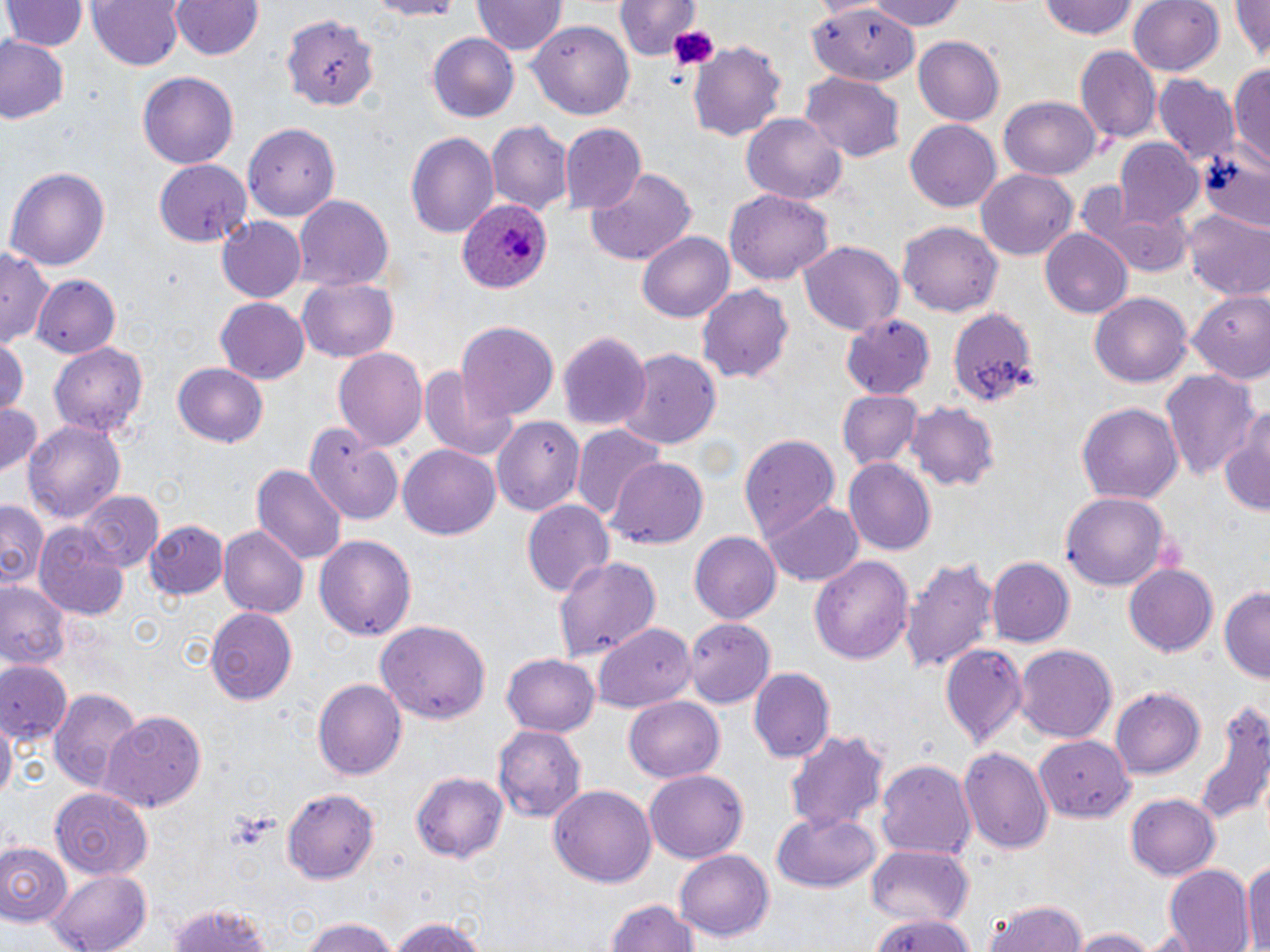

Approximate bounding boxes as named x1/y1/x2/y2 corners in pixels. Platelet locations: (x1=665, y1=22, x2=722, y2=73). Uninfected red blood cell locations: (x1=5, y1=0, x2=84, y2=53), (x1=87, y1=0, x2=184, y2=72), (x1=169, y1=0, x2=266, y2=61), (x1=858, y1=0, x2=973, y2=29), (x1=1037, y1=0, x2=1142, y2=42), (x1=1128, y1=0, x2=1225, y2=76), (x1=1232, y1=0, x2=1270, y2=66), (x1=472, y1=1, x2=566, y2=58), (x1=615, y1=1, x2=700, y2=63), (x1=805, y1=6, x2=922, y2=83), (x1=283, y1=16, x2=379, y2=114), (x1=530, y1=20, x2=635, y2=119), (x1=427, y1=33, x2=521, y2=123), (x1=913, y1=34, x2=1005, y2=124), (x1=0, y1=35, x2=69, y2=125), (x1=686, y1=39, x2=788, y2=139), (x1=1075, y1=46, x2=1161, y2=143), (x1=1228, y1=64, x2=1270, y2=171), (x1=135, y1=71, x2=239, y2=169), (x1=798, y1=73, x2=905, y2=163), (x1=1154, y1=76, x2=1240, y2=169), (x1=999, y1=96, x2=1100, y2=181), (x1=740, y1=109, x2=847, y2=207), (x1=243, y1=119, x2=338, y2=260), (x1=905, y1=119, x2=1004, y2=211), (x1=488, y1=120, x2=572, y2=218), (x1=562, y1=125, x2=647, y2=213), (x1=405, y1=130, x2=500, y2=242), (x1=1113, y1=137, x2=1205, y2=227), (x1=1200, y1=155, x2=1270, y2=234), (x1=153, y1=160, x2=248, y2=247), (x1=5, y1=165, x2=110, y2=273), (x1=976, y1=168, x2=1079, y2=261), (x1=585, y1=169, x2=696, y2=267), (x1=725, y1=190, x2=832, y2=284), (x1=1081, y1=191, x2=1197, y2=274), (x1=292, y1=194, x2=393, y2=292), (x1=1183, y1=210, x2=1270, y2=302), (x1=217, y1=216, x2=307, y2=301), (x1=899, y1=223, x2=1003, y2=316), (x1=1040, y1=228, x2=1131, y2=318), (x1=637, y1=231, x2=734, y2=322), (x1=798, y1=239, x2=902, y2=334), (x1=0, y1=244, x2=53, y2=352), (x1=32, y1=274, x2=120, y2=359), (x1=298, y1=277, x2=399, y2=362), (x1=696, y1=286, x2=793, y2=382), (x1=1188, y1=288, x2=1270, y2=385), (x1=1089, y1=291, x2=1193, y2=387), (x1=215, y1=298, x2=309, y2=384), (x1=943, y1=303, x2=1038, y2=411), (x1=840, y1=314, x2=938, y2=398), (x1=456, y1=321, x2=559, y2=419), (x1=558, y1=329, x2=649, y2=433), (x1=0, y1=340, x2=27, y2=420), (x1=50, y1=340, x2=149, y2=438), (x1=615, y1=347, x2=723, y2=451), (x1=331, y1=348, x2=428, y2=451), (x1=171, y1=362, x2=268, y2=448), (x1=418, y1=363, x2=518, y2=463), (x1=1163, y1=369, x2=1262, y2=483), (x1=836, y1=388, x2=923, y2=468), (x1=0, y1=400, x2=43, y2=479), (x1=1077, y1=401, x2=1182, y2=507), (x1=909, y1=404, x2=1000, y2=493), (x1=1218, y1=407, x2=1270, y2=516), (x1=491, y1=415, x2=583, y2=515), (x1=24, y1=419, x2=125, y2=527), (x1=305, y1=423, x2=404, y2=522), (x1=572, y1=426, x2=665, y2=520), (x1=737, y1=432, x2=840, y2=539), (x1=53, y1=438, x2=157, y2=554), (x1=397, y1=444, x2=500, y2=540), (x1=609, y1=456, x2=708, y2=551), (x1=844, y1=458, x2=936, y2=555), (x1=252, y1=465, x2=345, y2=566), (x1=76, y1=490, x2=164, y2=573), (x1=1060, y1=492, x2=1171, y2=592), (x1=521, y1=499, x2=613, y2=598), (x1=761, y1=500, x2=864, y2=586), (x1=0, y1=501, x2=47, y2=590), (x1=148, y1=518, x2=229, y2=600), (x1=33, y1=524, x2=130, y2=618), (x1=218, y1=525, x2=308, y2=620), (x1=689, y1=530, x2=782, y2=624), (x1=314, y1=536, x2=416, y2=639), (x1=551, y1=554, x2=661, y2=662), (x1=903, y1=554, x2=998, y2=677), (x1=810, y1=555, x2=914, y2=665), (x1=988, y1=557, x2=1075, y2=647), (x1=1123, y1=564, x2=1218, y2=657), (x1=0, y1=578, x2=72, y2=673), (x1=1218, y1=586, x2=1270, y2=683), (x1=205, y1=607, x2=297, y2=706), (x1=684, y1=617, x2=775, y2=707), (x1=374, y1=618, x2=491, y2=725), (x1=593, y1=624, x2=697, y2=714), (x1=939, y1=644, x2=1026, y2=749), (x1=1015, y1=644, x2=1118, y2=741), (x1=501, y1=652, x2=599, y2=735), (x1=0, y1=661, x2=71, y2=745), (x1=748, y1=668, x2=835, y2=764), (x1=313, y1=678, x2=405, y2=780), (x1=48, y1=685, x2=143, y2=791), (x1=1110, y1=687, x2=1205, y2=778), (x1=624, y1=697, x2=723, y2=783), (x1=1194, y1=701, x2=1270, y2=830), (x1=100, y1=710, x2=206, y2=811), (x1=1, y1=716, x2=16, y2=805), (x1=495, y1=724, x2=587, y2=823), (x1=1038, y1=724, x2=1142, y2=824), (x1=786, y1=729, x2=889, y2=834), (x1=961, y1=747, x2=1053, y2=856), (x1=874, y1=755, x2=976, y2=858), (x1=409, y1=769, x2=507, y2=863), (x1=641, y1=769, x2=749, y2=862), (x1=548, y1=782, x2=657, y2=888), (x1=282, y1=787, x2=382, y2=883), (x1=52, y1=790, x2=152, y2=881), (x1=1124, y1=794, x2=1221, y2=880), (x1=770, y1=810, x2=883, y2=893), (x1=0, y1=840, x2=72, y2=925), (x1=863, y1=845, x2=973, y2=928), (x1=676, y1=850, x2=774, y2=942), (x1=1242, y1=860, x2=1269, y2=951), (x1=1160, y1=864, x2=1254, y2=951), (x1=45, y1=868, x2=154, y2=952), (x1=981, y1=898, x2=1089, y2=952), (x1=164, y1=900, x2=280, y2=952), (x1=605, y1=900, x2=700, y2=952), (x1=868, y1=914, x2=978, y2=952), (x1=385, y1=915, x2=491, y2=952), (x1=297, y1=917, x2=406, y2=952), (x1=1067, y1=926, x2=1163, y2=952). Plasmodium ovale-infected red blood cell locations: (x1=457, y1=198, x2=551, y2=297). Slide-level diagnosis: Plasmodium ovale. Thin blood film. Image is 1270×952 pixels. May-Grünwald-Giemsa stain. Light microscopy. Captured at 1000x magnification. Single field of view.